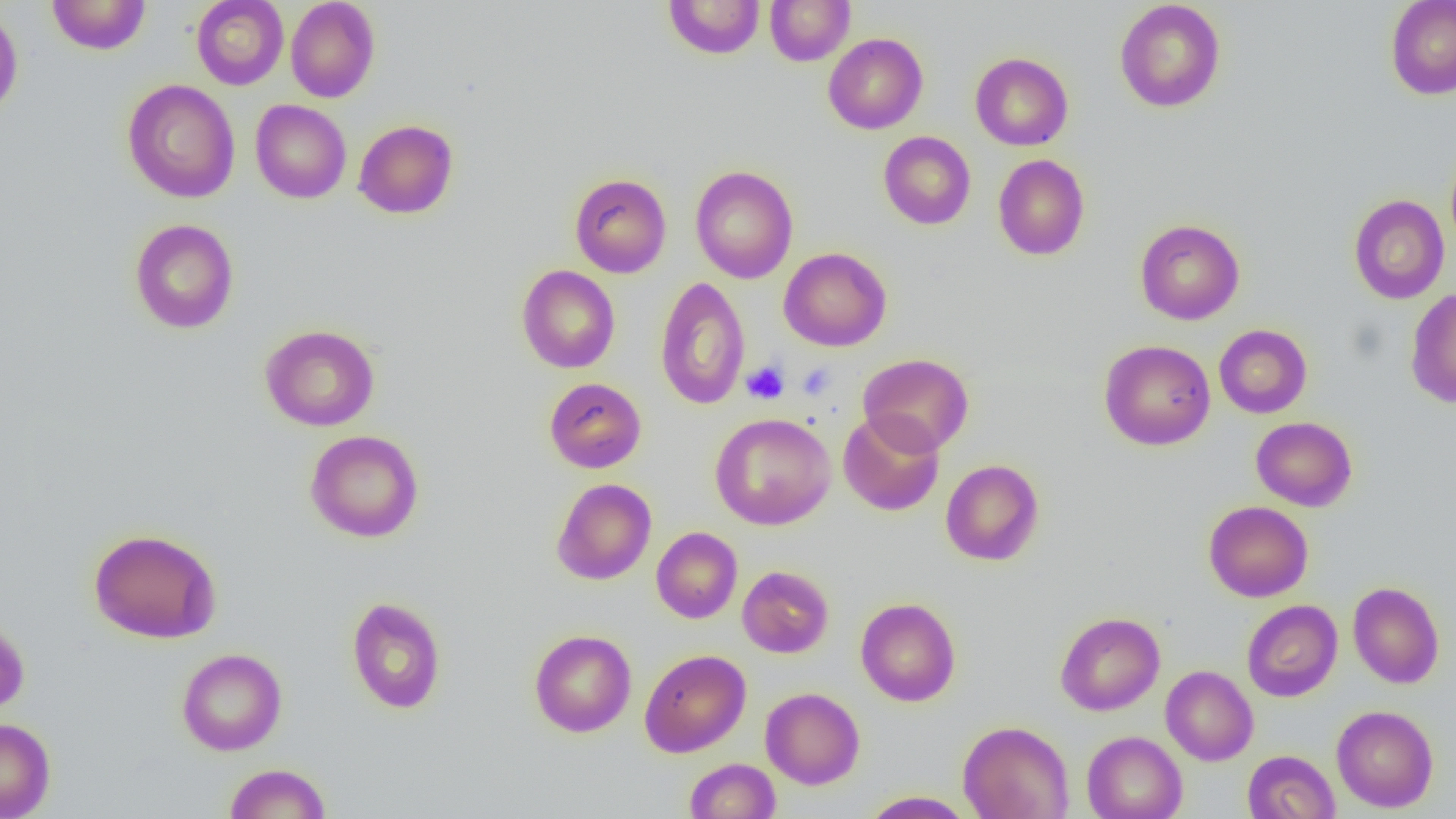
Approximate bounding boxes as (x1, y1, x2, y2) in pixels. Uninfected red blood cell locations: (46, 0, 152, 55), (191, 0, 289, 90), (285, 0, 380, 103), (663, 0, 765, 59), (764, 0, 855, 66), (1386, 0, 1456, 99), (1114, 1, 1226, 112), (0, 7, 24, 121), (823, 33, 928, 134), (970, 52, 1073, 150), (122, 79, 240, 203), (250, 99, 352, 203), (353, 119, 458, 219), (878, 131, 976, 229), (993, 154, 1090, 260), (690, 165, 798, 284), (569, 173, 671, 277), (1349, 195, 1449, 303), (129, 218, 239, 334), (1135, 219, 1245, 324), (778, 247, 891, 351), (516, 265, 620, 373), (654, 276, 751, 411), (1405, 287, 1456, 408), (260, 324, 380, 431), (1214, 324, 1312, 418), (1099, 339, 1216, 450), (858, 353, 974, 456), (543, 377, 647, 473), (709, 412, 836, 530), (838, 412, 944, 516), (1251, 417, 1357, 511), (304, 430, 424, 543), (940, 459, 1045, 566), (551, 478, 656, 585), (1203, 500, 1313, 602), (88, 527, 222, 644), (651, 527, 742, 623), (737, 565, 834, 658), (1347, 581, 1445, 689), (346, 596, 446, 714), (855, 597, 961, 706), (1242, 600, 1343, 701), (1054, 611, 1165, 716), (0, 616, 29, 716), (529, 628, 637, 737), (176, 648, 287, 755), (639, 649, 751, 756), (1160, 665, 1258, 765), (760, 687, 865, 789), (1331, 705, 1439, 812), (0, 718, 56, 818), (958, 720, 1074, 819), (1082, 730, 1188, 819), (1242, 750, 1340, 818), (684, 758, 781, 818), (223, 763, 331, 818), (859, 790, 975, 818). Platelet locations: (741, 361, 789, 405), (797, 362, 836, 400). Slide-level diagnosis: negative for blood parasites. 1000x magnification. Image is 1456×819 pixels. One field of a larger specimen. Light microscopy. Thin blood film.